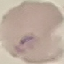

Malaria status: uninfected. Thin smear of blood. Giemsa-stained preparation. Acquired by smartphone through the microscope eyepiece. Cell patch, automatically extracted from a larger field of view and resized to 64 × 64 pixels.